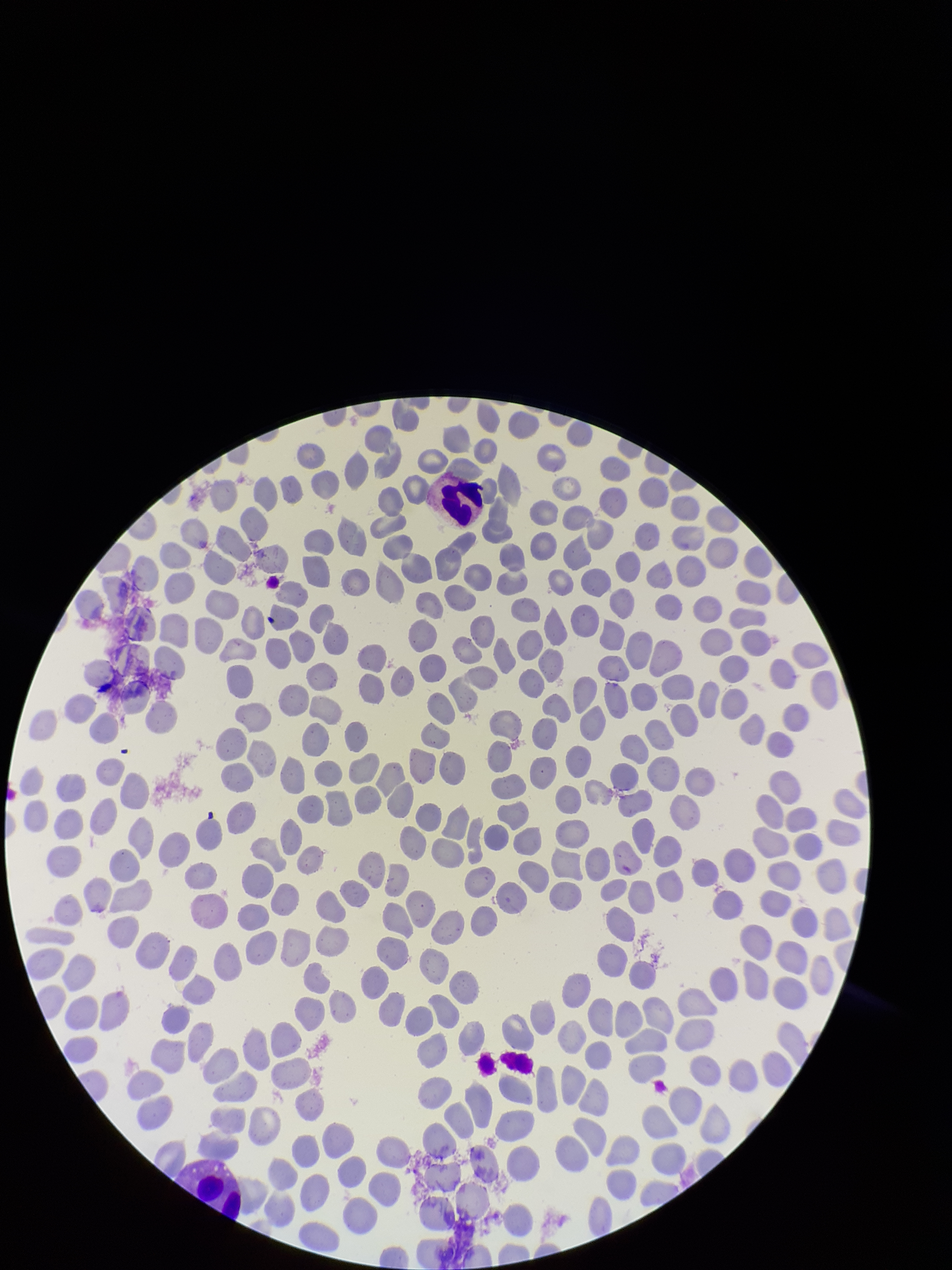
image size = 952×1270 pixels
parasitized red blood cell count = 0
preparation = thin
stain = Giemsa
red blood cell count = 335
field of view = one from this slide
parasitized red blood cells = none detected
capture = smartphone photograph through the microscope eyepiece
patient malaria status = negative